Identify the parasite.
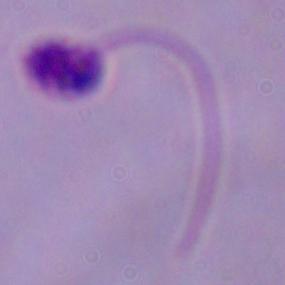

This is Leishmania.

Summary:
  - Modality: micrograph
  - Magnification: 1000x